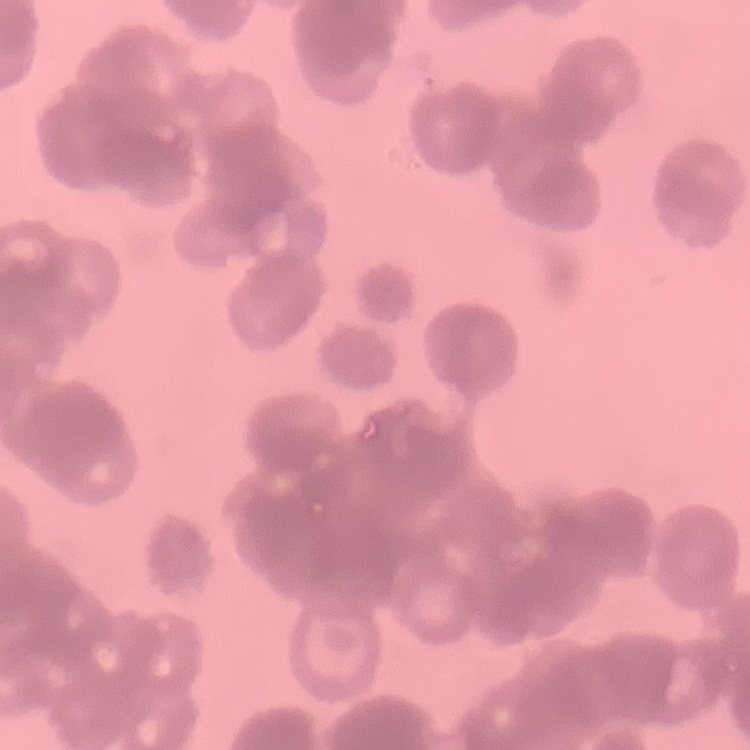 The erythrocytes show rouleaux formation. Field's or Giemsa stain. Square crop of a larger photomicrograph. Thin blood smear.